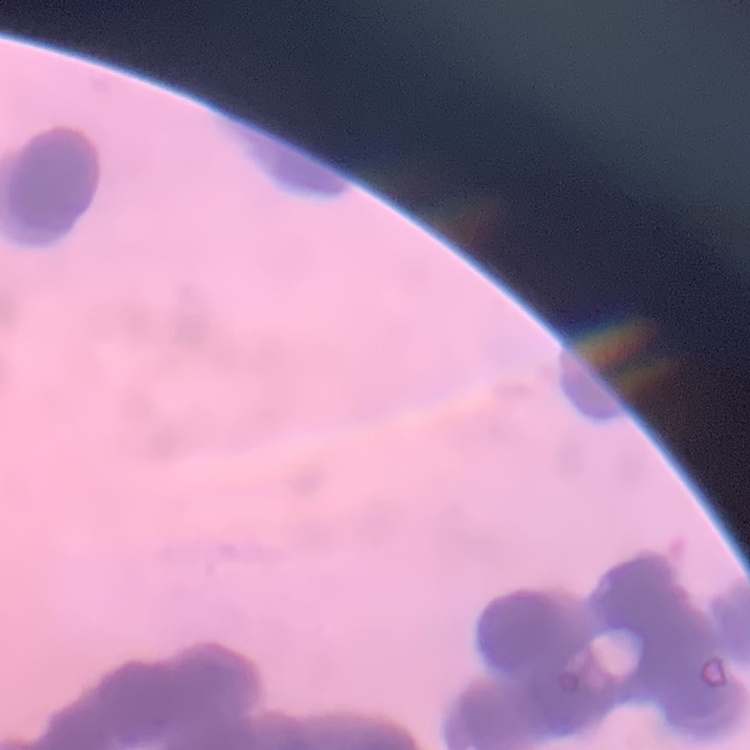
Summary:
  - Red blood cell morphology: rouleaux formation
  - Stain: Field's or Giemsa
  - Preparation: thin blood smear
  - Image type: square crop of a larger photomicrograph